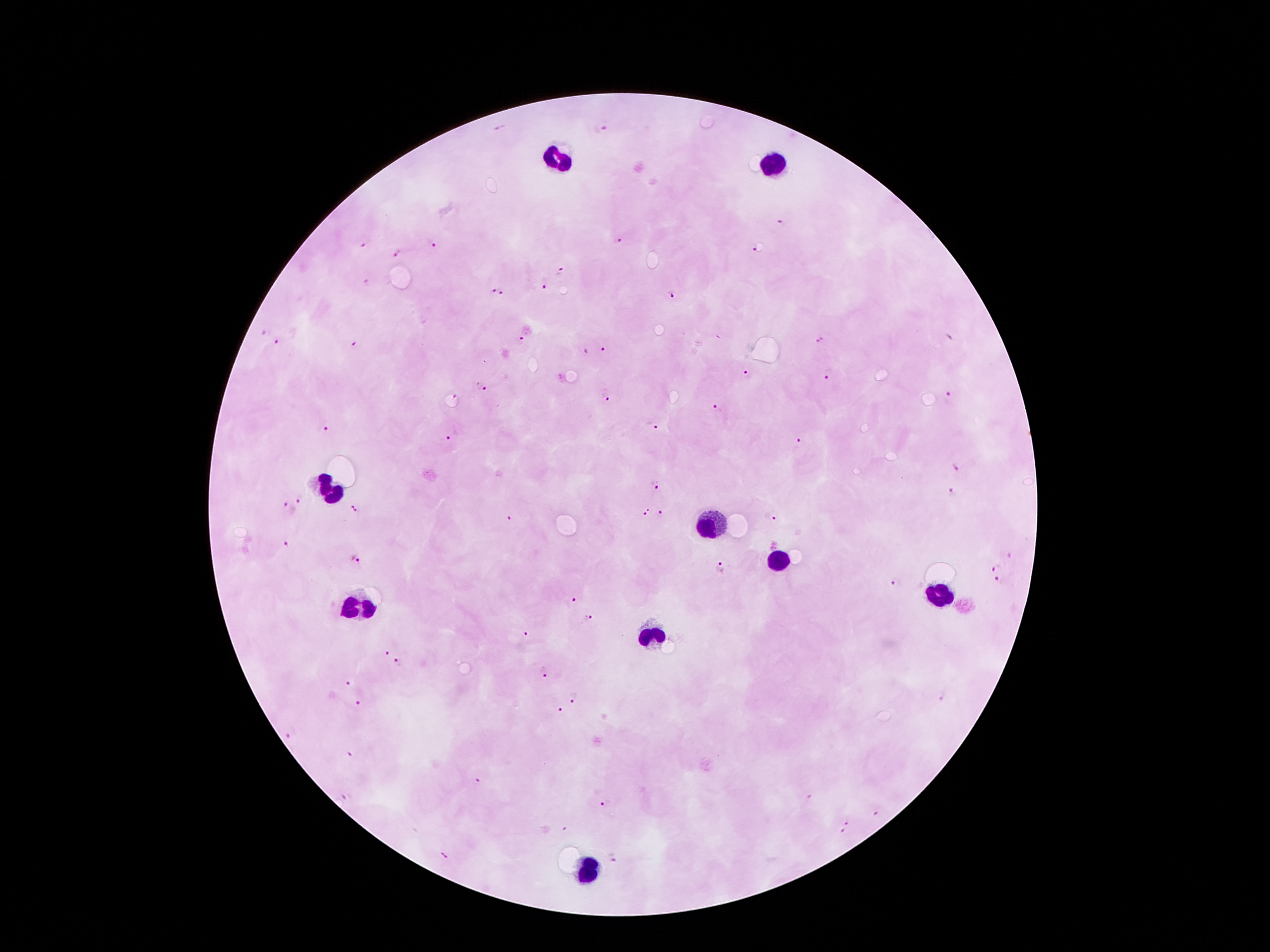
Approximate centers as {x, y} in pixels.
Summary:
  - Malaria parasite locations: {500, 128}, {600, 128}, {781, 222}, {617, 241}, {431, 243}, {363, 245}, {755, 250}, {398, 254}, {561, 271}, {366, 281}, {545, 283}, {503, 290}, {492, 291}, {672, 294}, {262, 330}, {521, 339}, {819, 340}, {277, 343}, {354, 344}, {604, 348}, {749, 376}, {828, 376}, {482, 387}, {455, 395}, {605, 397}, {949, 397}, {716, 409}, {653, 424}, {325, 426}, {451, 437}, {799, 442}, {956, 467}, {655, 485}, {952, 493}, {301, 498}, {357, 509}, {288, 510}, {647, 512}, {660, 514}, {770, 516}, {508, 519}, {288, 543}, {1010, 556}, {357, 558}, {721, 568}, {997, 568}, {898, 583}, {1000, 584}, {573, 600}, {588, 618}, {525, 634}, {385, 652}, {398, 661}, {541, 671}, {350, 684}, {575, 698}, {362, 704}, {561, 712}, {293, 732}, {352, 753}, {478, 781}, {346, 795}, {606, 801}, {877, 814}, {849, 821}, {565, 830}, {843, 833}, {447, 857}, {617, 859}
  - Leukocyte locations: {560, 159}, {778, 165}, {333, 495}, {711, 523}, {778, 560}, {942, 593}, {356, 609}, {652, 636}, {583, 871}
  - Image size: 1270×952 pixels
  - Preparation: thick blood smear
  - Stain: Giemsa
  - Patient malaria status: infected with Plasmodium falciparum
  - Field of view: one from this slide
  - Capture: smartphone through the microscope eyepiece
  - Magnification: 100x